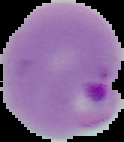 From a thin blood smear. Malaria status: parasitized. Image is 124×142 pixels. Cell region segmented out of the field of view; the surrounding area is masked to black.